Name the parasite shown.
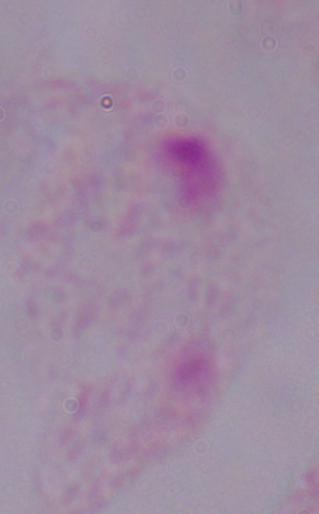
A trichomonad.

1000x magnification. Micrograph.